Classify this cell by malaria status.
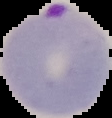
It is parasitized.

preparation = thin blood smear
image type = cell region segmented out of the field of view; surrounding area masked to black
image size = 112×118 pixels